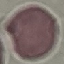
Summary:
  - Result: negative for malaria parasites
  - Capture: smartphone through the microscope eyepiece
  - Image type: cell patch, automatically extracted from a larger field of view and resized to 64 × 64 pixels
  - Preparation: thin blood smear
  - Stain: Giemsa